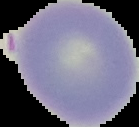

Summary:
  - Malaria status: uninfected
  - Image type: segmented cell region on a black background
  - Image size: 139×127 pixels
  - Preparation: thin blood smear